Describe the morphology of the erythrocytes.
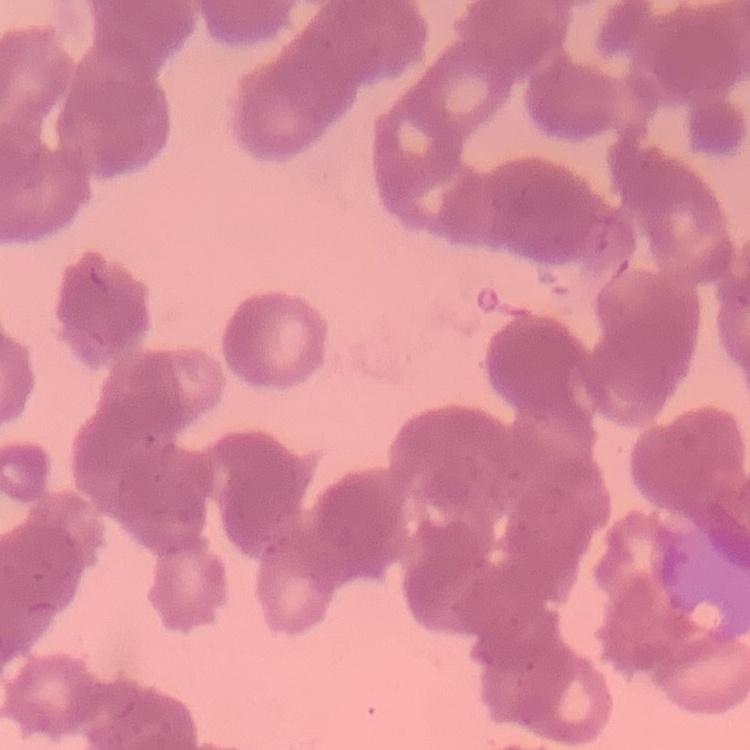
Rouleaux formation.

Summary:
  - Preparation: thin blood film
  - Image type: one tile cut from a larger photomicrograph
  - Stain: Field's or Giemsa